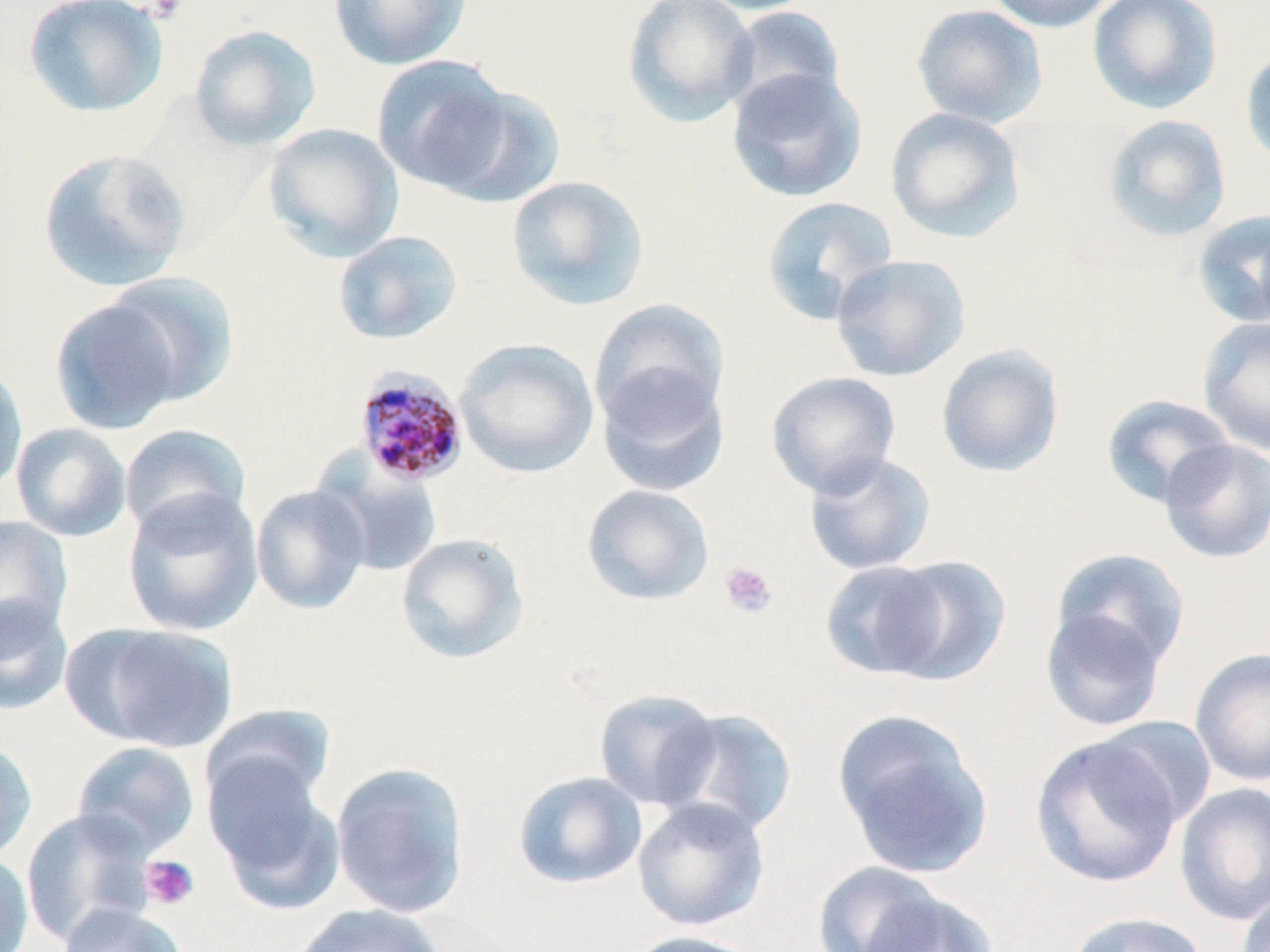

Plasmodium malariae-infected red blood cell locations = approximate bounding boxes as [x1, y1, x2, y2] in pixels: [355, 366, 470, 489]
slide-level diagnosis = Plasmodium malariae
stain = May-Grünwald-Giemsa
modality = optical microscopy
magnification = 1000x
platelet locations = approximate bounding boxes as [x1, y1, x2, y2] in pixels: [719, 561, 778, 619], [140, 855, 200, 910]
field of view = one of a larger specimen
image size = 1270×952 pixels
preparation = thin blood smear
uninfected red blood cell locations = approximate bounding boxes as [x1, y1, x2, y2] in pixels: [22, 0, 169, 120], [329, 0, 472, 71], [623, 0, 759, 128], [690, 0, 820, 15], [982, 0, 1120, 33], [1087, 0, 1223, 116], [723, 4, 845, 116], [911, 4, 1048, 128], [189, 24, 321, 151], [1240, 45, 1270, 170], [371, 54, 517, 193], [726, 67, 868, 203], [433, 85, 567, 209], [884, 107, 1026, 243], [1102, 114, 1232, 244], [262, 123, 404, 261], [37, 148, 192, 293], [505, 175, 650, 311], [759, 196, 897, 325], [1190, 208, 1270, 329], [333, 230, 464, 345], [829, 254, 971, 382], [101, 271, 240, 407], [49, 297, 185, 435], [589, 298, 731, 429], [1197, 316, 1270, 456], [454, 338, 600, 478], [935, 343, 1065, 478], [0, 357, 29, 496], [595, 362, 731, 499], [766, 370, 902, 498], [1100, 394, 1236, 509], [10, 422, 132, 542], [119, 424, 252, 538], [1157, 438, 1270, 564], [802, 451, 938, 576], [313, 453, 443, 578], [581, 484, 715, 606], [250, 485, 371, 615], [122, 489, 263, 636], [0, 515, 73, 647], [394, 532, 531, 665], [1051, 548, 1192, 672], [868, 555, 1012, 686], [0, 595, 74, 716], [1039, 602, 1172, 731], [69, 622, 239, 753], [1189, 646, 1270, 787], [593, 688, 723, 810], [199, 703, 337, 819], [661, 708, 799, 837], [832, 710, 995, 878], [1095, 715, 1218, 831], [1030, 734, 1183, 890], [0, 736, 37, 866], [71, 740, 201, 859], [204, 755, 344, 913], [330, 762, 470, 919], [512, 771, 648, 890], [1174, 782, 1270, 926], [632, 797, 771, 932], [21, 809, 156, 947], [0, 852, 34, 952], [812, 861, 951, 952], [856, 888, 999, 952], [1236, 890, 1270, 952], [56, 902, 186, 952], [290, 904, 448, 952], [1065, 911, 1211, 952], [622, 930, 765, 952]